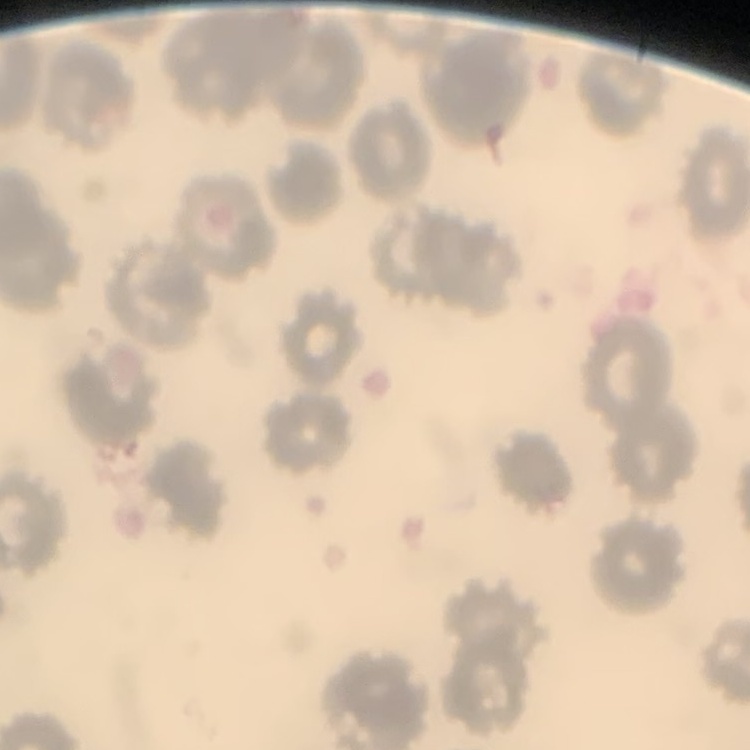
The erythrocytes exhibit no rouleaux formation. Stained with either Field's or Giemsa. Square crop of a larger photomicrograph. Thin blood smear.